Evaluate for malaria.
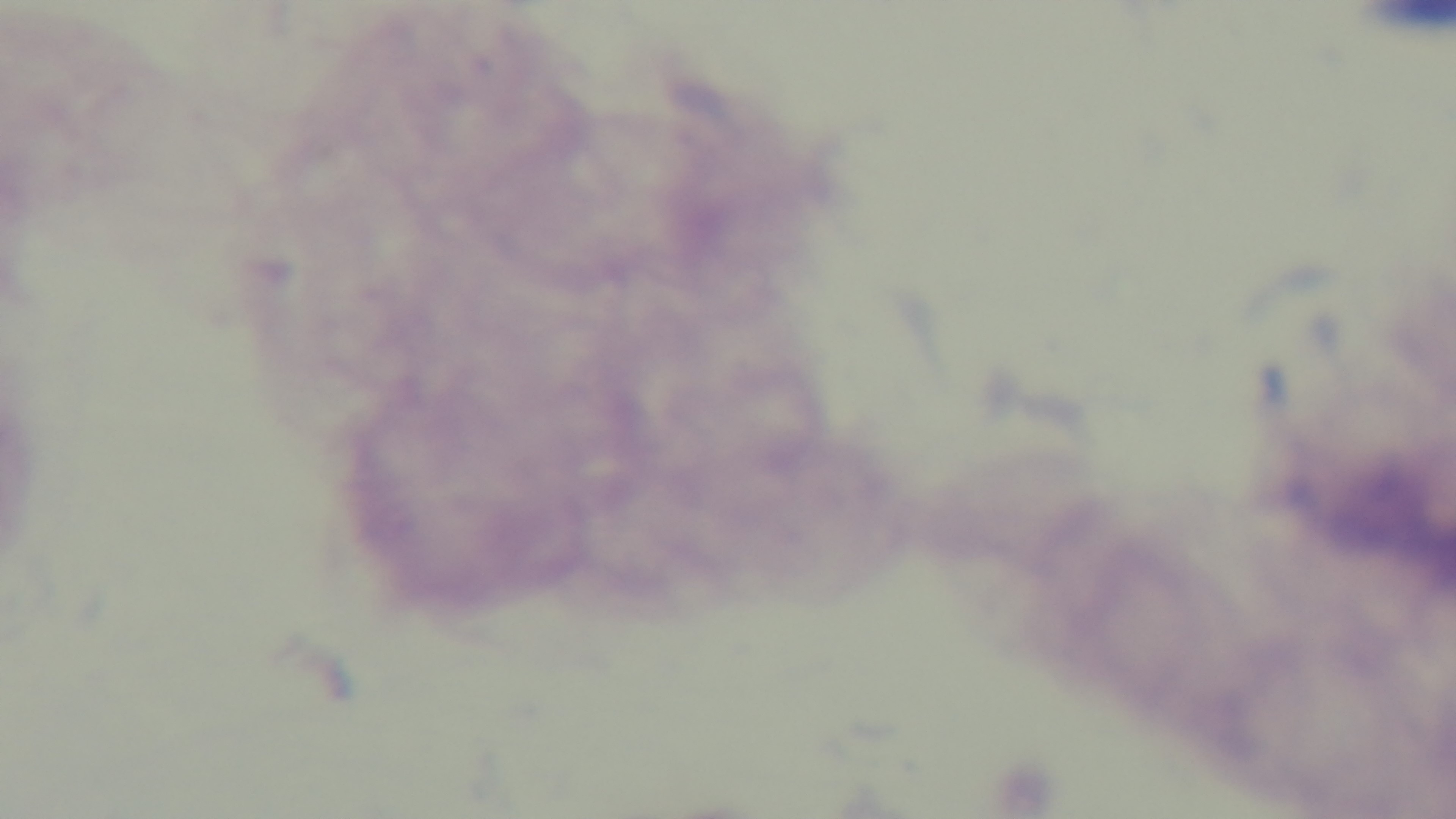
Negative.

field of view = single
preparation = thick smear
modality = light microscopy
objective = 100x oil immersion
capture = mounted 4K digital camera
stain = Giemsa